Name the parasite shown.
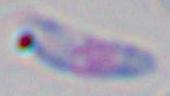

This is Toxoplasma gondii.

Micrograph. Captured at 1000x magnification.